Identify the blood parasite species.
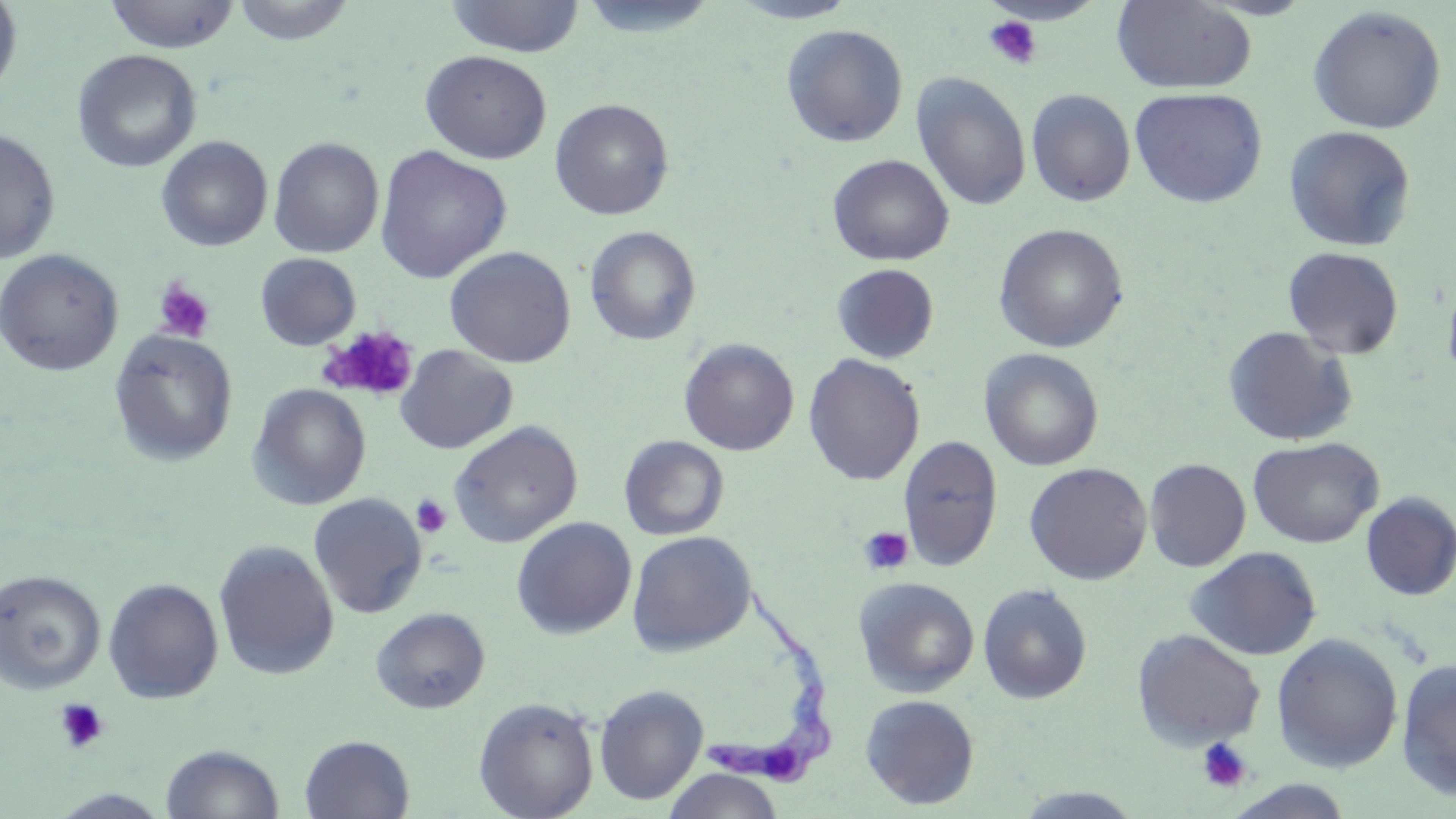

Trypanosoma brucei.

Approximate bounding boxes as [x1, y1, x2, y2] in pixels. Platelet locations: [983, 15, 1042, 70], [153, 278, 216, 343], [321, 325, 419, 402], [411, 494, 453, 539], [858, 526, 914, 576], [54, 698, 109, 754], [1196, 737, 1253, 794]. Uninfected red blood cell locations: [231, 0, 357, 45], [445, 0, 584, 58], [575, 0, 722, 40], [729, 0, 862, 24], [1111, 0, 1257, 94], [0, 1, 23, 100], [104, 1, 240, 52], [1308, 6, 1447, 134], [781, 24, 909, 148], [72, 49, 202, 173], [420, 50, 552, 164], [911, 72, 1031, 212], [1129, 87, 1267, 208], [1026, 89, 1135, 207], [550, 98, 674, 220], [1282, 125, 1417, 252], [0, 127, 60, 264], [156, 136, 273, 252], [268, 137, 383, 258], [374, 145, 512, 283], [827, 154, 954, 266], [993, 223, 1129, 353], [584, 225, 702, 346], [444, 246, 576, 368], [1283, 247, 1404, 359], [0, 249, 124, 376], [255, 253, 361, 350], [832, 263, 940, 364], [1442, 271, 1456, 390], [1223, 325, 1358, 446], [109, 329, 238, 466], [679, 338, 799, 456], [394, 344, 518, 454], [980, 348, 1103, 471], [803, 353, 925, 486], [248, 383, 371, 510], [448, 420, 583, 547], [898, 434, 1003, 571], [619, 435, 729, 541], [1247, 436, 1383, 548], [1144, 458, 1251, 572], [1024, 462, 1152, 585], [1360, 491, 1456, 601], [308, 493, 427, 619], [511, 517, 637, 639], [627, 530, 756, 656], [213, 540, 339, 680], [1185, 546, 1322, 661], [0, 568, 105, 693], [103, 577, 224, 704], [854, 577, 980, 698], [977, 582, 1092, 705], [371, 606, 490, 714], [1132, 628, 1266, 751], [1271, 633, 1403, 773], [1396, 659, 1456, 800], [594, 684, 708, 805], [860, 694, 980, 809], [473, 697, 599, 818], [299, 734, 414, 818], [160, 743, 284, 819], [663, 768, 784, 818], [1010, 788, 1146, 818], [48, 789, 173, 819]. Trypanosoma brucei locations: [702, 579, 838, 790]. Thin blood film. Optical microscopy. 1000x magnification. May-Grünwald-Giemsa-stained preparation. One field of a larger specimen. Image is 1456×819 pixels.